Report the malaria status of this cell.
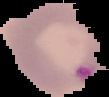
Parasitized.

From a thin blood film. The area outside the segmented cell region is set to black. Image is 109×97 pixels.